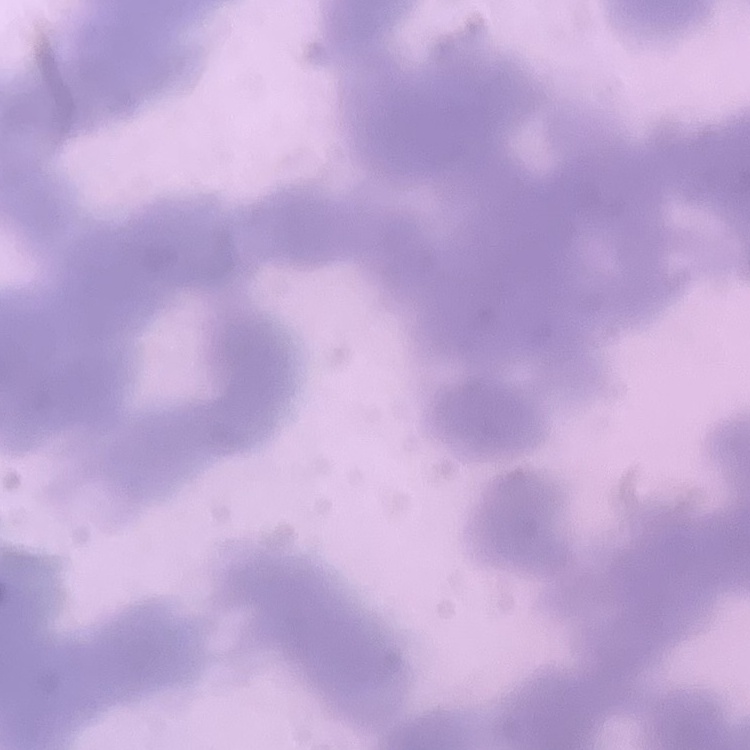 The red blood cells exhibit rouleaux formation. Square crop of a larger photomicrograph. Stained with either Field's or Giemsa. Thin blood film.